Locate every blood parasite and identify its species.
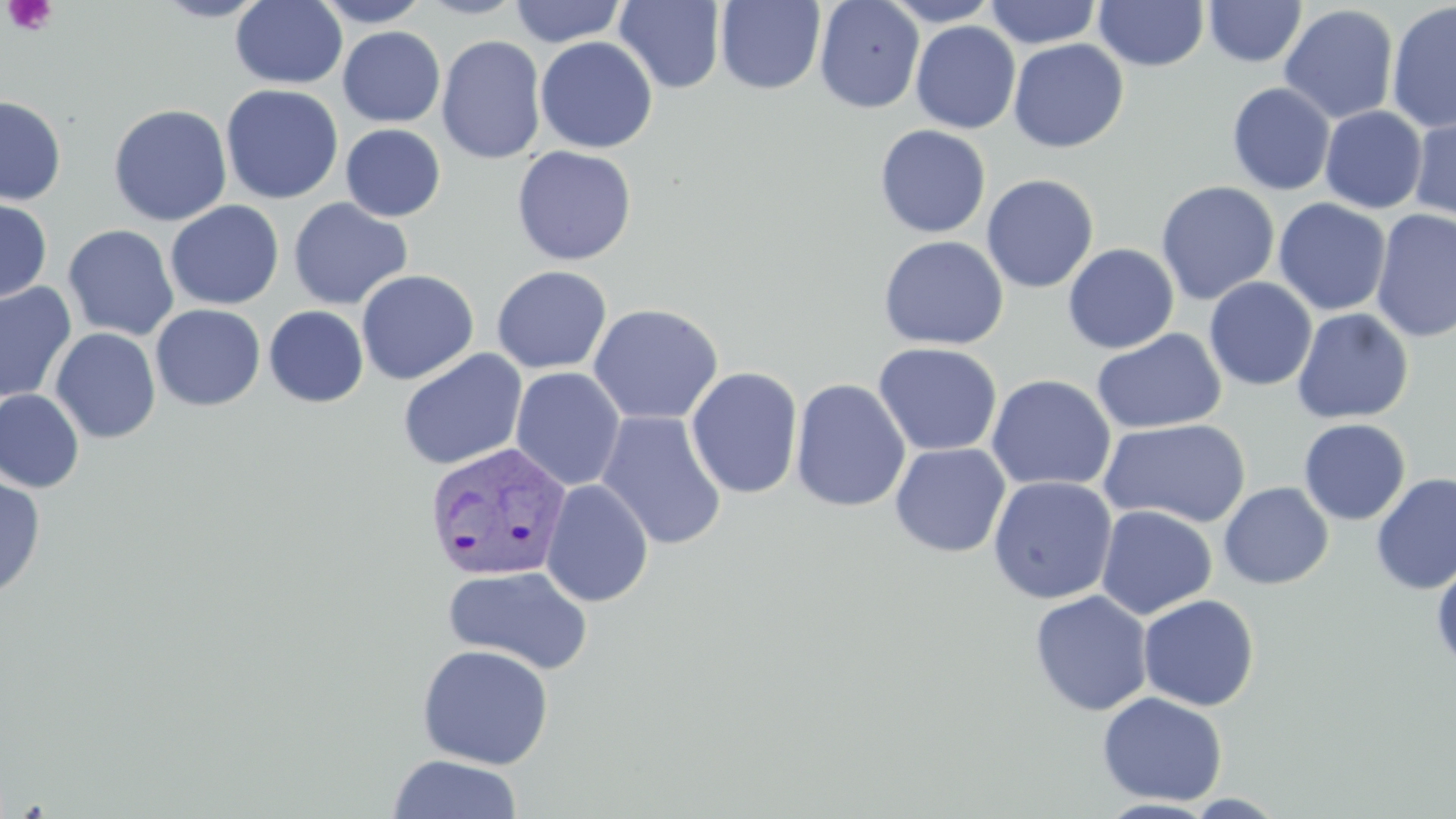

Approximate bounding boxes as (x1,y1)-(x2,y2) corner pairs in pixels.
Plasmodium vivax-infected red blood cells: (423,441)-(573,584).
No Plasmodium falciparum, Plasmodium ovale, Plasmodium malariae, Babesia divergens, or Trypanosoma brucei observed.

Uninfected red blood cell locations: (152,0)-(272,22), (230,0)-(347,89), (311,0)-(432,27), (415,0)-(528,19), (509,0)-(627,47), (715,0)-(826,95), (814,0)-(925,114), (881,0)-(1002,26), (984,0)-(1102,49), (1203,0)-(1306,67), (614,1)-(726,94), (1094,1)-(1209,71), (1386,2)-(1456,133), (1279,4)-(1399,124), (910,21)-(1021,134), (338,26)-(445,127), (436,35)-(547,164), (534,36)-(658,154), (1008,38)-(1129,153), (1227,82)-(1335,195), (221,84)-(343,204), (0,95)-(67,206), (108,103)-(232,226), (1320,106)-(1427,213), (1408,109)-(1456,226), (340,124)-(446,222), (874,125)-(991,238), (512,145)-(637,265), (981,174)-(1099,294), (1156,181)-(1279,305), (0,197)-(52,304), (287,198)-(413,310), (1273,198)-(1392,316), (165,200)-(284,310), (1370,209)-(1456,343), (63,225)-(179,341), (878,235)-(1009,351), (1063,243)-(1179,354), (491,265)-(613,374), (356,269)-(479,385), (1204,277)-(1317,391), (0,282)-(77,404), (587,303)-(724,426), (151,304)-(265,411), (263,305)-(369,408), (1291,308)-(1414,425), (50,327)-(161,444), (1091,328)-(1227,435), (872,341)-(1003,457), (398,349)-(527,471), (685,366)-(803,500), (511,367)-(626,491), (986,374)-(1117,492), (790,377)-(911,513), (0,388)-(85,493), (596,410)-(727,551), (1098,419)-(1251,529), (1297,419)-(1411,525), (890,443)-(1011,557), (1370,472)-(1456,595), (0,475)-(46,599), (987,476)-(1118,604), (540,479)-(654,607), (1218,481)-(1334,589), (1096,505)-(1218,620), (1431,560)-(1456,672), (442,564)-(593,675), (1029,590)-(1153,717), (1138,594)-(1260,710), (417,643)-(554,769), (1097,691)-(1228,806), (387,753)-(523,818), (1182,793)-(1288,818), (1095,798)-(1219,818). Platelet locations: (2,0)-(58,37). Slide-level diagnosis: Plasmodium vivax. May-Grünwald-Giemsa-stained preparation. Image is 1456×819 pixels. Thin blood film. Light microscopy. Captured at 1000x magnification. One field of a larger specimen.